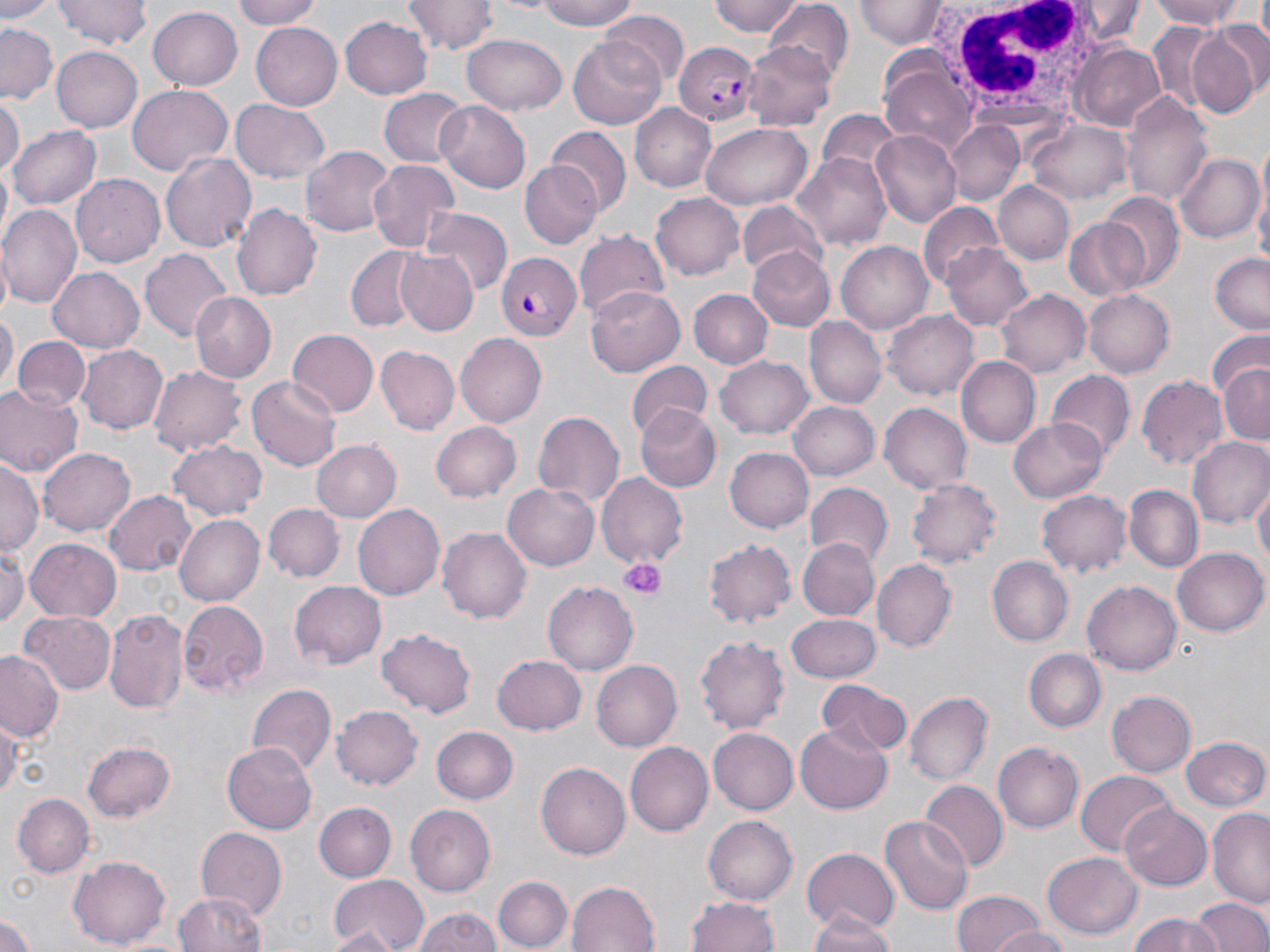
Summary:
  - Coordinate format: approximate bounding boxes as [x1, y1, x2, y2] in pixels
  - Plasmodium falciparum-infected red blood cell locations: [675, 40, 760, 125], [496, 253, 580, 339]
  - Uninfected red blood cell locations: [0, 0, 55, 24], [54, 0, 150, 50], [230, 0, 329, 29], [529, 0, 645, 30], [710, 0, 803, 38], [1080, 0, 1142, 42], [1148, 0, 1249, 28], [403, 1, 495, 54], [854, 2, 948, 48], [764, 4, 854, 83], [149, 5, 244, 89], [599, 11, 687, 91], [340, 17, 432, 100], [250, 21, 343, 109], [0, 23, 57, 103], [1188, 23, 1267, 118], [1144, 24, 1227, 117], [461, 35, 567, 116], [569, 36, 669, 129], [742, 40, 835, 131], [1071, 44, 1168, 131], [50, 45, 141, 133], [880, 66, 976, 149], [127, 84, 233, 175], [379, 87, 468, 169], [1122, 91, 1212, 210], [0, 99, 22, 179], [231, 100, 329, 183], [437, 102, 532, 195], [629, 104, 716, 192], [1033, 121, 1132, 204], [946, 122, 1022, 205], [700, 123, 812, 209], [9, 124, 101, 211], [550, 130, 631, 214], [871, 132, 961, 227], [299, 144, 393, 242], [161, 151, 257, 252], [793, 152, 894, 251], [1176, 153, 1264, 243], [367, 158, 460, 253], [520, 160, 604, 248], [71, 172, 165, 264], [998, 182, 1073, 264], [1255, 184, 1269, 283], [1099, 190, 1183, 286], [651, 193, 746, 279], [232, 203, 321, 302], [738, 203, 830, 284], [2, 204, 83, 307], [917, 205, 1004, 291], [422, 206, 510, 296], [1063, 217, 1155, 303], [573, 229, 670, 324], [836, 240, 934, 333], [942, 242, 1034, 332], [347, 246, 427, 331], [394, 248, 480, 337], [748, 248, 837, 330], [140, 249, 231, 343], [1210, 253, 1269, 336], [46, 267, 144, 354], [585, 285, 686, 375], [995, 288, 1089, 378], [689, 289, 774, 369], [1084, 290, 1174, 376], [188, 294, 274, 382], [1, 308, 17, 392], [885, 310, 979, 402], [806, 317, 887, 409], [287, 329, 379, 419], [1205, 329, 1269, 416], [455, 331, 546, 424], [14, 336, 89, 414], [78, 344, 168, 434], [378, 346, 459, 433], [716, 355, 813, 439], [957, 357, 1039, 449], [628, 361, 712, 441], [1218, 361, 1269, 445], [149, 363, 246, 457], [1048, 370, 1135, 462], [1136, 373, 1228, 467], [247, 375, 341, 472], [0, 383, 84, 478], [788, 400, 879, 481], [879, 402, 972, 492], [635, 405, 721, 492], [530, 408, 625, 508], [1008, 417, 1108, 502], [432, 422, 520, 502], [1189, 437, 1270, 531], [312, 439, 402, 521], [170, 440, 265, 520], [39, 445, 135, 534], [725, 446, 813, 531], [0, 461, 42, 555], [597, 473, 688, 569], [907, 479, 1002, 568], [504, 481, 600, 571], [1253, 481, 1269, 571], [806, 483, 893, 567], [1124, 486, 1204, 575], [1038, 489, 1131, 578], [104, 490, 197, 575], [266, 504, 343, 582], [354, 505, 444, 599], [172, 513, 267, 607], [437, 525, 531, 623], [797, 536, 878, 621], [25, 539, 122, 622], [704, 539, 796, 627], [0, 545, 27, 631], [1173, 545, 1269, 637], [986, 554, 1073, 646], [874, 559, 956, 652], [290, 581, 388, 669], [544, 581, 637, 674], [1083, 581, 1181, 675], [178, 600, 270, 695], [103, 609, 188, 714], [20, 611, 117, 695], [786, 612, 882, 681], [377, 628, 475, 718], [694, 634, 790, 735], [1026, 648, 1106, 733], [0, 651, 64, 741], [491, 653, 587, 735], [591, 658, 682, 753], [815, 678, 911, 760], [246, 683, 335, 777], [906, 690, 992, 784], [1108, 691, 1195, 778], [332, 704, 422, 789], [0, 714, 20, 807], [794, 725, 891, 813], [432, 726, 518, 804], [708, 727, 798, 815], [1179, 737, 1270, 813], [225, 740, 321, 833], [82, 741, 176, 822], [625, 742, 713, 836], [993, 742, 1085, 834], [535, 762, 630, 860], [1074, 769, 1175, 856], [922, 779, 1005, 868], [13, 793, 94, 876], [313, 802, 397, 882], [1119, 803, 1213, 891], [405, 805, 495, 897], [1208, 808, 1270, 907], [880, 814, 973, 915], [704, 816, 797, 903], [196, 828, 287, 916], [802, 849, 898, 935], [1043, 851, 1143, 939], [68, 855, 169, 948], [495, 873, 573, 950], [326, 874, 430, 952], [565, 879, 658, 952], [947, 890, 1050, 952], [174, 891, 268, 952], [688, 896, 783, 952], [1193, 897, 1269, 952], [410, 908, 503, 952], [0, 910, 38, 952], [804, 913, 898, 952], [1126, 913, 1222, 952], [991, 924, 1070, 952], [322, 927, 399, 952]
  - Platelet locations: [621, 557, 663, 600]
  - White blood cell locations: [921, 2, 1112, 118]
  - Slide-level diagnosis: Plasmodium falciparum
  - Preparation: thin blood smear
  - Magnification: 1000x
  - Modality: light microscopy
  - Stain: May-Grünwald-Giemsa
  - Field of view: single
  - Image size: 1270×952 pixels